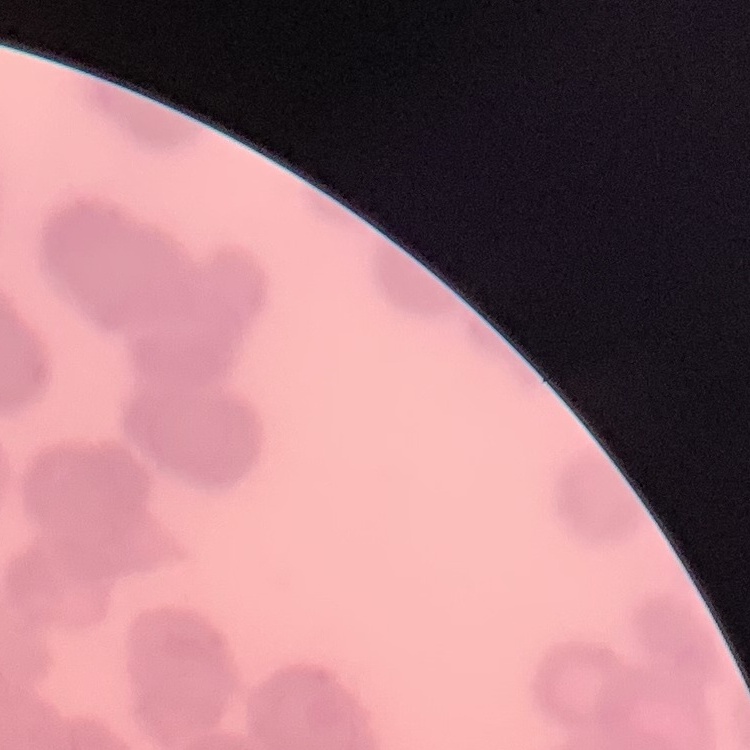
erythrocyte_morphology: rouleaux formation
preparation: thin peripheral smear
stain: Field's or Giemsa
image_type: one tile cut from a larger photomicrograph